Assess this cell for malaria.
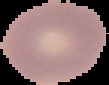

Uninfected.

image size = 109×85 pixels
preparation = thin blood film
image type = segmented cell region with the area outside set to black